Look for Plasmodium parasites.
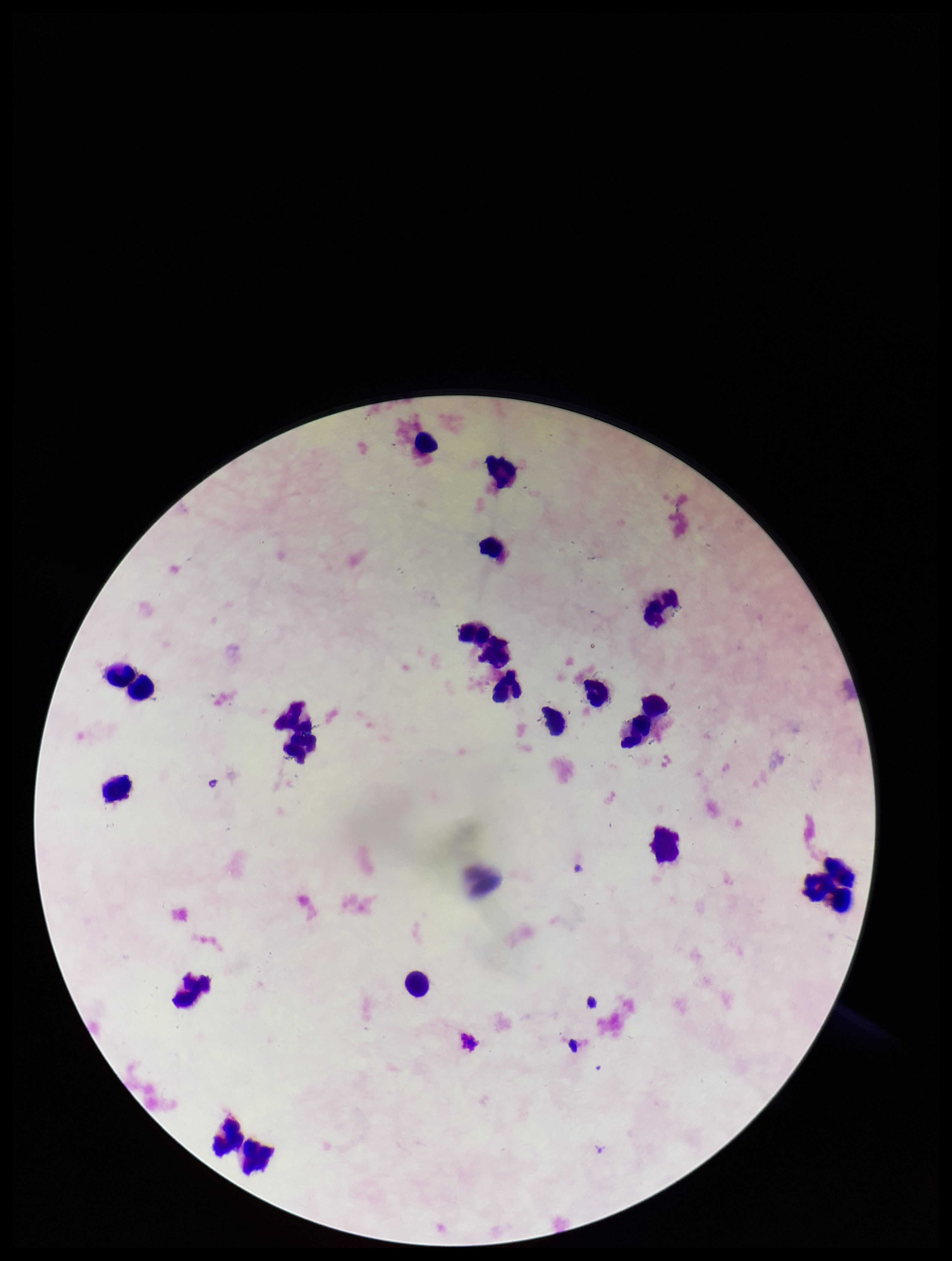

None identified.

capture = smartphone photograph through the microscope eyepiece
preparation = thick
stain = Giemsa
image size = 952×1261 pixels
leukocyte count = 22
field of view = single
patient malaria status = negative
parasite count = 0